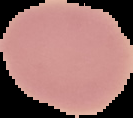
Summary:
  - Image size: 133×118 pixels
  - Malaria status: uninfected
  - Preparation: thin blood smear
  - Image type: segmented cell region with the area outside set to black